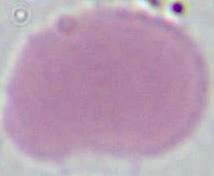

identification: erythrocyte
magnification: 1000x
modality: photomicrograph